Give the position of every leukocyte visible.
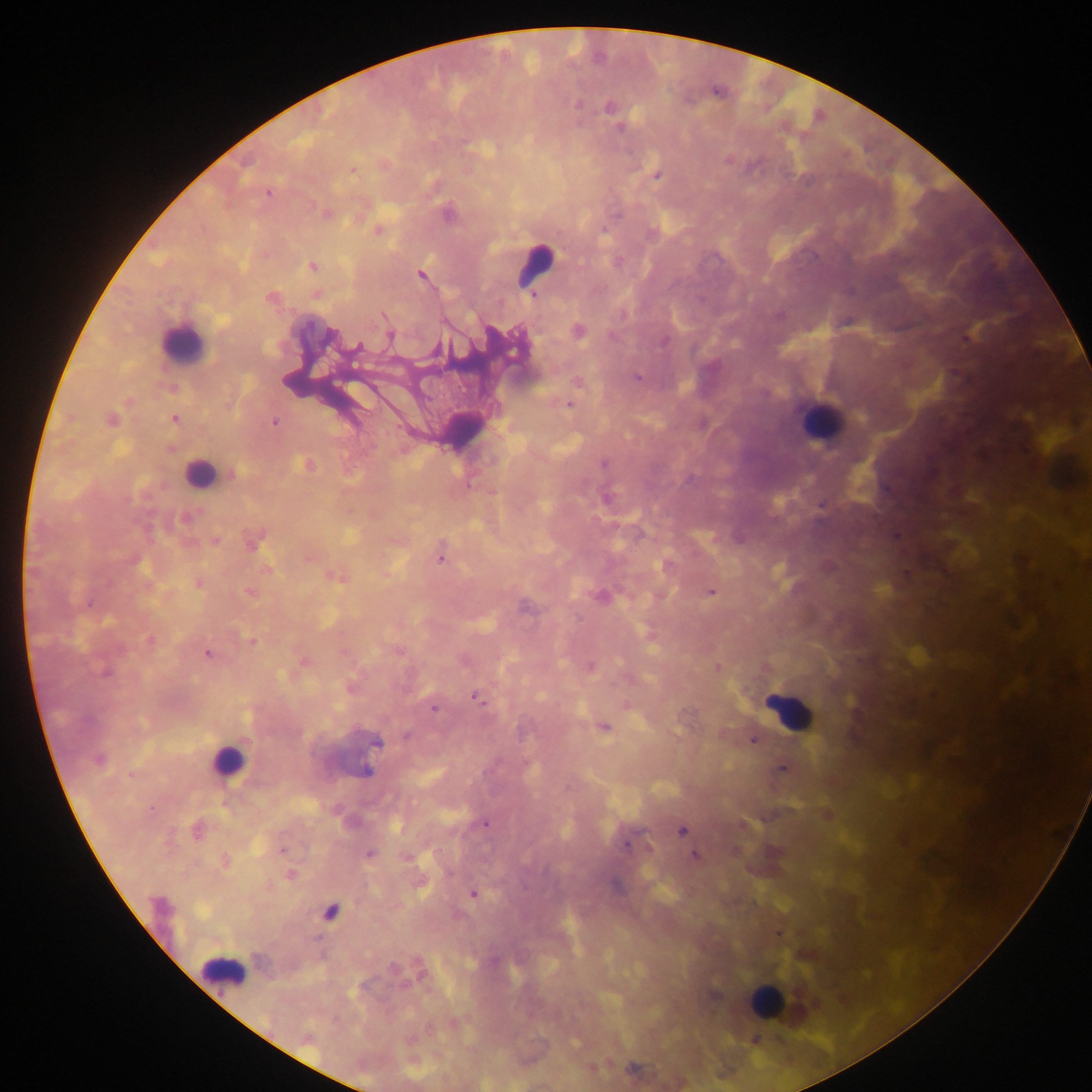
Approximate centers as (x, y) in pixels.
Leukocytes: (535, 264), (182, 343), (820, 421), (200, 473), (790, 712), (226, 762), (222, 969), (765, 1000).

Summary:
  - Malaria parasite locations: (577, 104), (609, 107), (620, 128), (353, 171), (657, 176), (268, 193), (326, 213), (448, 213), (378, 230), (313, 266), (420, 275), (534, 297), (272, 298), (623, 314), (778, 316), (578, 331), (390, 336), (332, 337), (664, 341), (358, 348), (636, 377), (577, 382), (569, 404), (175, 419), (111, 421), (274, 422), (604, 464), (305, 465), (232, 474), (606, 498), (821, 505), (185, 518), (217, 540), (253, 542), (441, 558), (335, 577), (199, 584), (711, 591), (249, 592), (601, 596), (88, 605), (525, 607), (150, 641), (252, 642), (208, 654), (305, 661), (591, 666), (718, 668), (105, 673), (477, 698), (434, 708), (604, 728), (406, 736), (753, 741), (376, 743), (99, 760), (781, 769), (366, 771), (485, 824), (680, 831), (197, 832), (626, 845), (283, 849), (370, 854), (694, 855), (226, 861), (291, 875), (473, 894), (159, 905), (330, 912), (393, 968), (715, 995), (632, 1068)
  - Preparation: thick blood smear
  - Capture: mobile-phone photograph through a microscope
  - Field of view: single
  - Image size: 1092×1092 pixels
  - Country: Ghana